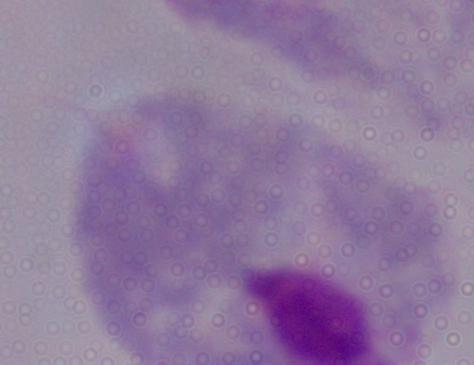
magnification = 1000x
modality = photomicrograph
identification = trichomonad